Give the extent of all white blood cells.
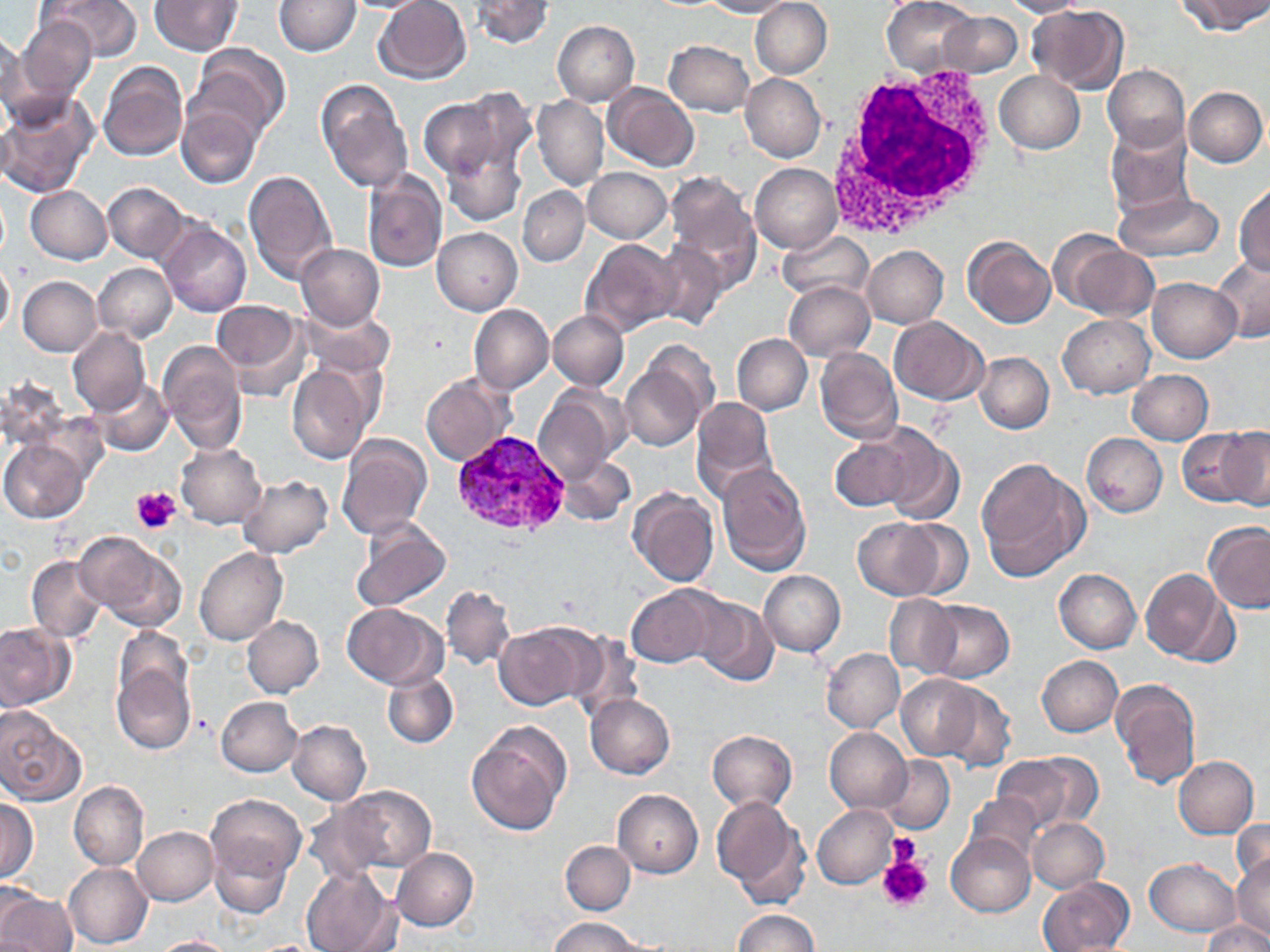

Approximate bounding boxes as (x1, y1, x2, y2) in pixels.
White blood cells: (822, 60, 1004, 243).

Summary:
  - Platelet locations: (132, 486, 181, 533), (886, 834, 921, 868), (877, 853, 932, 911)
  - Plasmodium vivax-infected red blood cell locations: (450, 428, 574, 541)
  - Uninfected red blood cell locations: (45, 0, 141, 62), (151, 0, 243, 54), (273, 0, 361, 56), (338, 0, 436, 13), (372, 0, 471, 84), (469, 0, 553, 49), (750, 0, 832, 79), (882, 0, 976, 77), (1000, 0, 1087, 18), (1177, 0, 1268, 36), (701, 1, 794, 17), (1029, 5, 1129, 95), (938, 11, 1022, 77), (17, 17, 97, 102), (552, 20, 640, 106), (1, 32, 34, 126), (666, 40, 753, 117), (189, 44, 289, 140), (97, 61, 188, 161), (1102, 64, 1190, 153), (995, 70, 1084, 154), (740, 73, 826, 162), (316, 81, 412, 191), (603, 83, 699, 170), (1184, 86, 1267, 167), (453, 88, 536, 176), (0, 92, 98, 198), (416, 96, 509, 178), (533, 96, 608, 190), (177, 103, 263, 189), (1103, 122, 1194, 219), (441, 144, 526, 227), (750, 163, 842, 254), (583, 166, 670, 243), (244, 169, 338, 286), (361, 171, 447, 275), (662, 174, 761, 287), (1234, 181, 1270, 277), (102, 182, 188, 261), (25, 186, 112, 264), (517, 186, 590, 266), (1113, 192, 1225, 261), (157, 220, 251, 317), (433, 228, 522, 314), (778, 229, 874, 304), (1057, 235, 1159, 321), (963, 236, 1056, 328), (580, 238, 681, 338), (649, 240, 729, 331), (296, 244, 385, 331), (861, 245, 948, 328), (1210, 253, 1270, 345), (0, 259, 13, 338), (93, 263, 176, 342), (18, 276, 102, 355), (1147, 277, 1241, 362), (783, 280, 875, 362), (211, 302, 306, 393), (469, 304, 553, 394), (298, 308, 394, 378), (548, 310, 628, 390), (1059, 314, 1155, 398), (889, 316, 988, 405), (67, 327, 149, 414), (732, 335, 812, 414), (158, 342, 248, 452), (814, 348, 902, 444), (620, 352, 710, 452), (974, 353, 1054, 433), (287, 362, 375, 463), (1127, 370, 1212, 445), (420, 372, 515, 466), (89, 378, 173, 454), (534, 389, 622, 481), (691, 397, 777, 500), (878, 427, 963, 527), (1180, 427, 1258, 511), (1220, 428, 1270, 510), (337, 433, 432, 540), (1082, 433, 1167, 517), (831, 435, 917, 512), (0, 438, 89, 523), (176, 443, 266, 529), (558, 454, 637, 525), (976, 458, 1086, 578), (716, 461, 812, 576), (237, 475, 333, 557), (628, 489, 720, 589), (352, 518, 452, 612), (852, 518, 946, 599), (891, 519, 973, 599), (1203, 522, 1270, 613), (76, 532, 187, 631), (195, 549, 288, 646), (26, 555, 110, 642), (1142, 568, 1236, 666), (1054, 569, 1141, 653), (758, 570, 846, 656), (441, 585, 515, 671), (625, 585, 723, 668), (882, 595, 961, 679), (690, 596, 778, 685), (923, 599, 1014, 682), (341, 603, 443, 689), (241, 615, 324, 698), (493, 621, 598, 709), (0, 623, 75, 712), (111, 626, 193, 712), (565, 633, 645, 723), (820, 648, 904, 733), (1037, 655, 1123, 737), (112, 662, 195, 754), (382, 671, 458, 749), (894, 674, 987, 762), (1110, 678, 1201, 789), (935, 680, 1016, 770), (586, 694, 675, 778), (216, 696, 303, 777), (0, 708, 85, 806), (287, 720, 371, 806), (465, 723, 569, 835), (825, 727, 910, 812), (706, 730, 796, 814), (990, 754, 1089, 832), (1172, 756, 1258, 838), (878, 757, 955, 834), (69, 781, 148, 871), (328, 785, 436, 875), (612, 788, 702, 878), (965, 793, 1041, 867), (205, 794, 306, 885), (710, 796, 810, 906), (0, 798, 38, 883), (812, 804, 897, 888), (1027, 818, 1108, 893), (1231, 818, 1270, 892), (133, 827, 218, 905), (209, 832, 296, 918), (947, 832, 1034, 917), (560, 840, 635, 914), (391, 848, 478, 932), (1232, 853, 1269, 945), (1145, 858, 1240, 936), (64, 863, 152, 949), (302, 867, 401, 952), (1038, 878, 1132, 951), (0, 890, 77, 952), (732, 909, 818, 952), (547, 916, 645, 952), (1203, 920, 1270, 951), (150, 935, 240, 952)
  - Slide-level diagnosis: Plasmodium vivax
  - Field of view: one of a larger specimen
  - Modality: optical microscopy
  - Stain: May-Grünwald-Giemsa
  - Preparation: thin blood film
  - Magnification: 1000x
  - Image size: 1270×952 pixels